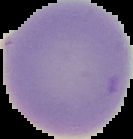

preparation = thin blood smear
image type = segmented cell region on a black background
image size = 133×139 pixels
result = no Plasmodium parasites seen